State which parasite is depicted.
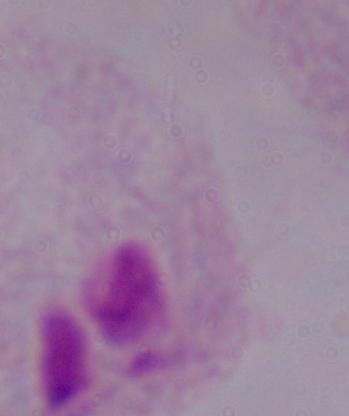
A trichomonad.

Summary:
  - Magnification: 1000x
  - Modality: photomicrograph